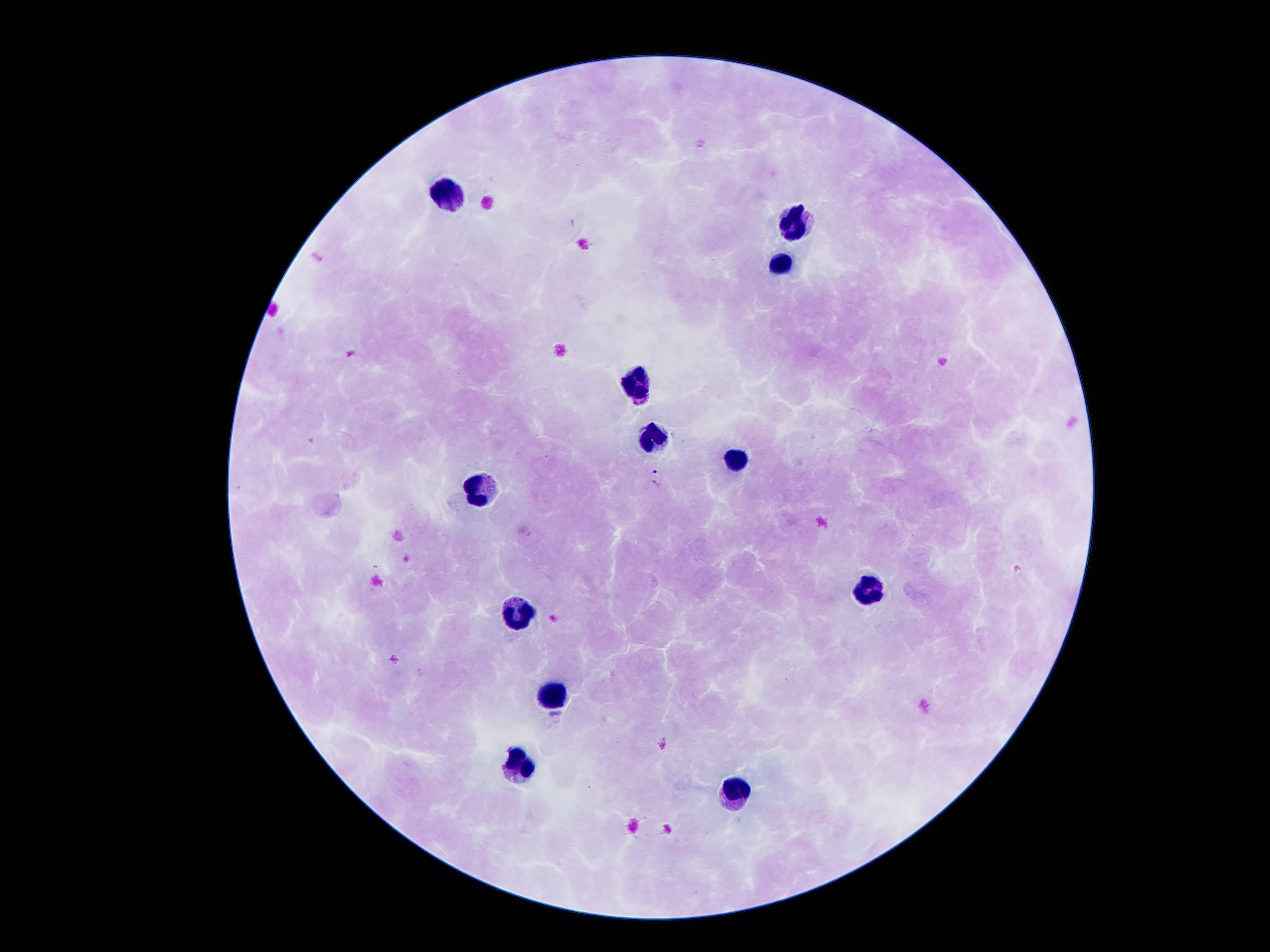
Approximate centers as {x, y} in pixels. Malaria parasite locations: {657, 477}, {1017, 569}. Leukocyte locations: {444, 198}, {795, 226}, {784, 261}, {637, 383}, {651, 435}, {734, 461}, {484, 491}, {871, 594}, {519, 615}, {551, 697}, {514, 765}, {736, 790}. Image is 1270×952 pixels. Single field of view. 100x magnification. Patient malaria status: infected with Plasmodium falciparum. Thick blood film. Giemsa-stained preparation. Smartphone photograph taken through the microscope eyepiece.